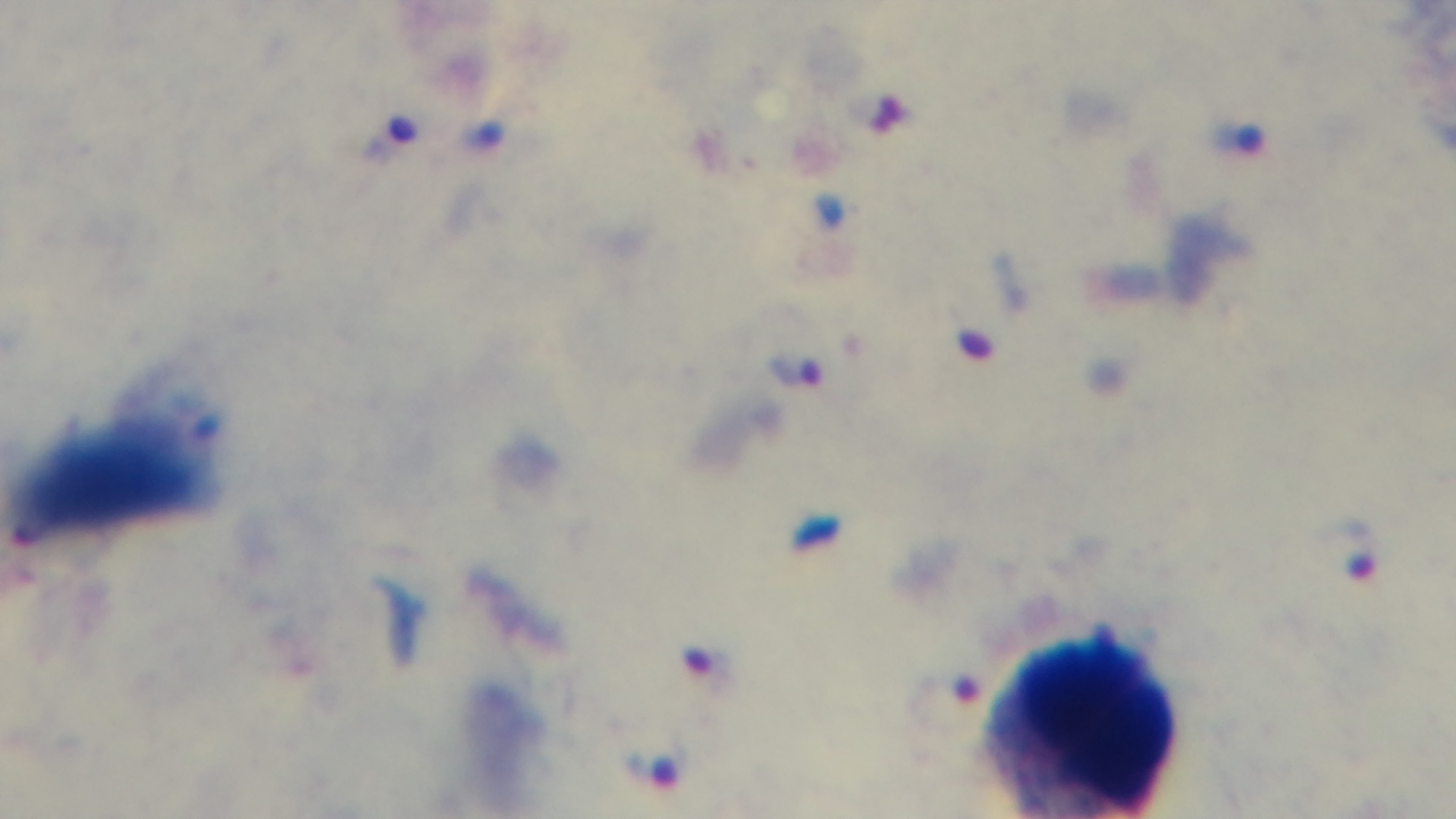

Summary:
  - Malaria status: positive
  - Stain: Giemsa
  - Modality: light microscopy
  - Objective: 100x oil immersion
  - Capture: mounted 4K digital camera
  - Field of view: one from the slide
  - Preparation: thick smear